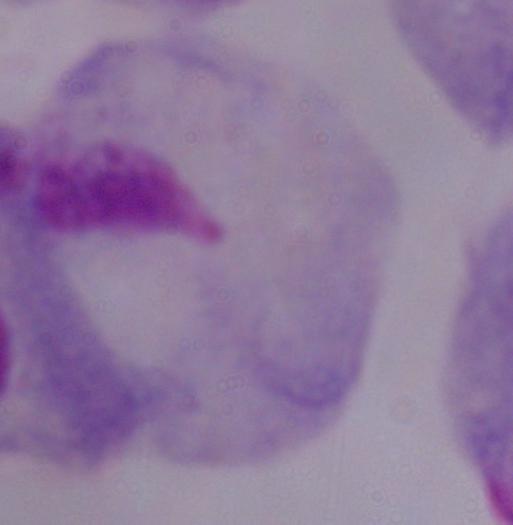

modality = photomicrograph
magnification = 1000x
identification = trichomonad